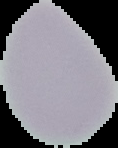 Image is 118×148 pixels. Result: no malaria parasites seen. Segmented cell region on a black background. From a thin blood film.